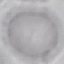
Summary:
  - Malaria status: uninfected
  - Image type: automatically extracted cell patch, resized to 64 × 64 pixels
  - Preparation: thin blood film
  - Stain: Giemsa
  - Capture: smartphone through the microscope eyepiece